Classify this cell by malaria status.
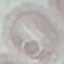
Uninfected.

Giemsa stain. Cell patch, automatically extracted from a larger field of view and resized to 64 × 64 pixels. Acquired by smartphone through the microscope eyepiece. Thin blood smear.